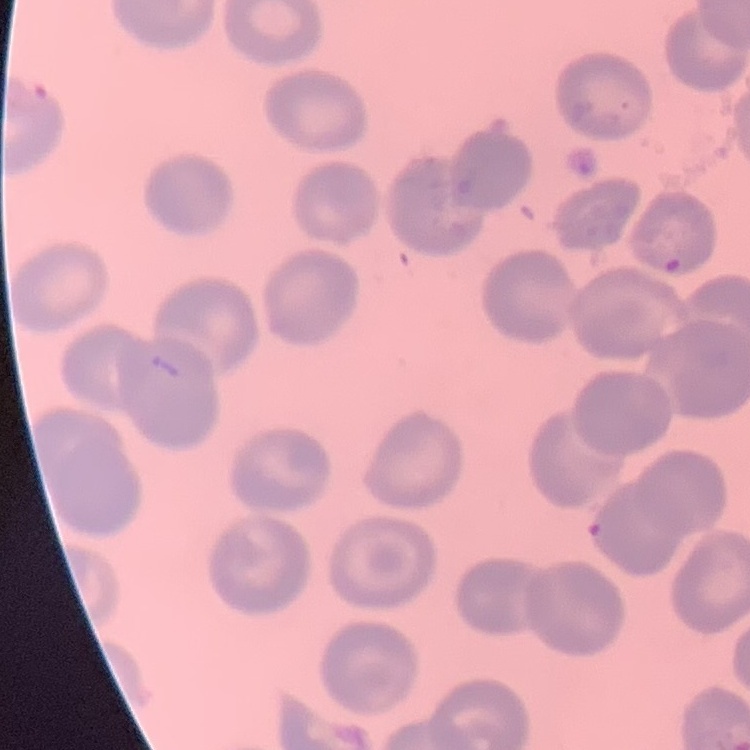
erythrocyte_morphology: no rouleaux formation
preparation: thin blood smear
stain: Field's or Giemsa
image_type: one tile cut from a larger photomicrograph